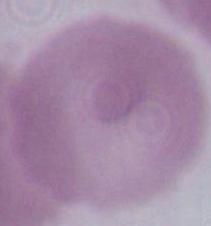
magnification = 1000x
modality = micrograph
identification = erythrocyte